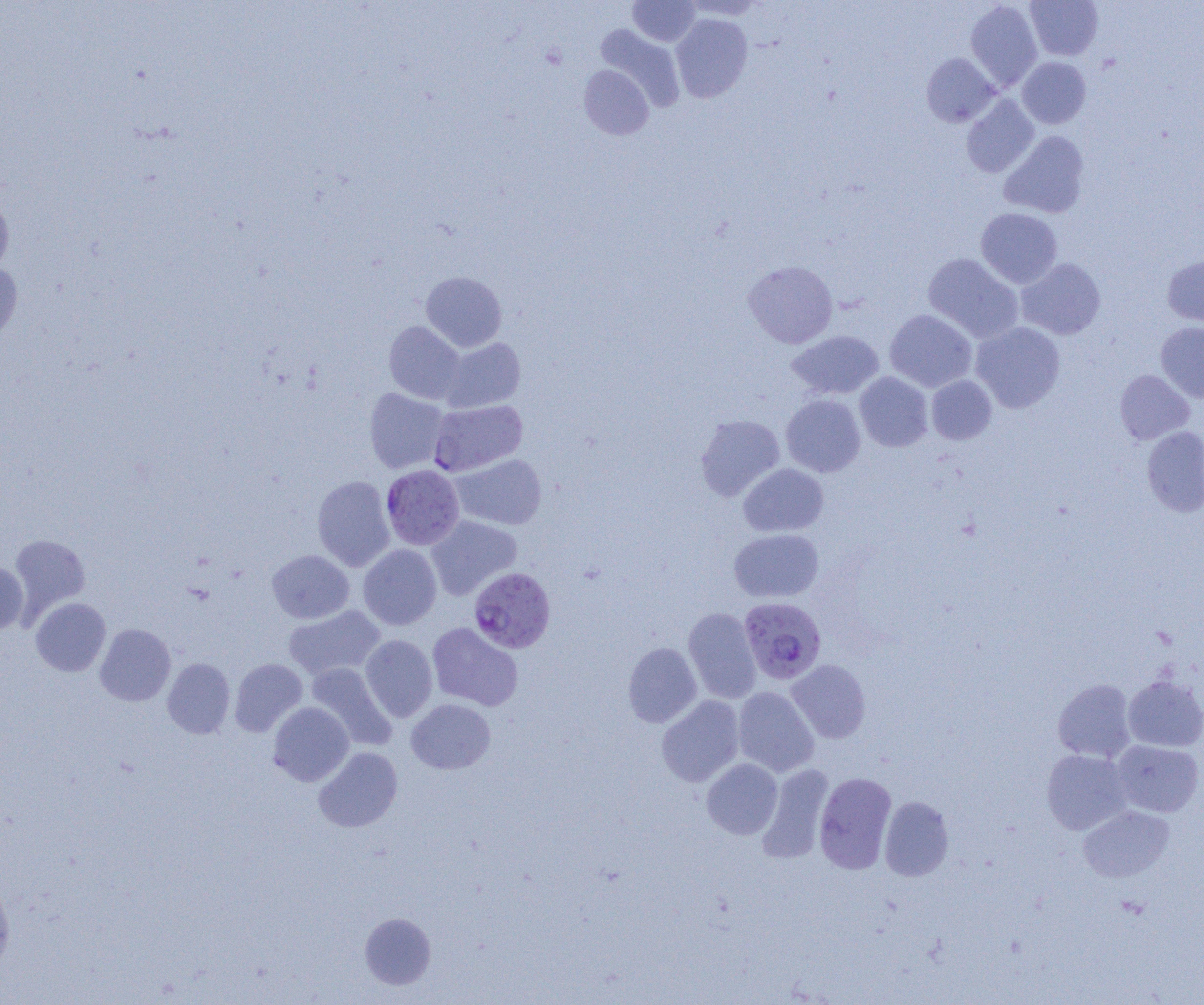

Summary:
  - Coordinate format: approximate bounding boxes as named x1/y1/x2/y2 corners in pixels
  - Uninfected red blood cell locations (subset): (x1=681, y1=0, x2=765, y2=20), (x1=1025, y1=0, x2=1103, y2=60), (x1=628, y1=1, x2=701, y2=46), (x1=965, y1=1, x2=1043, y2=91), (x1=671, y1=13, x2=753, y2=102), (x1=595, y1=24, x2=685, y2=112), (x1=922, y1=52, x2=999, y2=127), (x1=1017, y1=57, x2=1091, y2=128), (x1=579, y1=65, x2=654, y2=139), (x1=962, y1=95, x2=1039, y2=178), (x1=999, y1=131, x2=1090, y2=218), (x1=0, y1=193, x2=14, y2=280), (x1=976, y1=207, x2=1063, y2=288), (x1=923, y1=253, x2=1024, y2=343), (x1=1162, y1=254, x2=1204, y2=328), (x1=1016, y1=258, x2=1106, y2=340), (x1=743, y1=260, x2=838, y2=348), (x1=0, y1=262, x2=23, y2=355), (x1=421, y1=271, x2=507, y2=351), (x1=884, y1=309, x2=977, y2=391), (x1=384, y1=321, x2=465, y2=404), (x1=971, y1=321, x2=1065, y2=413), (x1=1155, y1=321, x2=1204, y2=403), (x1=786, y1=330, x2=884, y2=400), (x1=440, y1=338, x2=525, y2=412), (x1=1115, y1=369, x2=1194, y2=444), (x1=855, y1=372, x2=933, y2=451), (x1=926, y1=375, x2=997, y2=444), (x1=364, y1=388, x2=448, y2=473), (x1=781, y1=394, x2=865, y2=477), (x1=695, y1=414, x2=785, y2=501), (x1=1142, y1=425, x2=1204, y2=517), (x1=451, y1=454, x2=547, y2=530), (x1=738, y1=463, x2=828, y2=537), (x1=312, y1=475, x2=395, y2=571), (x1=426, y1=515, x2=522, y2=600), (x1=729, y1=529, x2=824, y2=603), (x1=9, y1=533, x2=90, y2=619), (x1=358, y1=544, x2=441, y2=630), (x1=267, y1=550, x2=354, y2=623), (x1=0, y1=561, x2=29, y2=633), (x1=30, y1=597, x2=111, y2=676), (x1=283, y1=605, x2=385, y2=680), (x1=683, y1=607, x2=762, y2=703), (x1=427, y1=622, x2=523, y2=711), (x1=95, y1=623, x2=175, y2=706), (x1=360, y1=635, x2=438, y2=721), (x1=623, y1=642, x2=702, y2=727), (x1=162, y1=658, x2=235, y2=738), (x1=230, y1=658, x2=307, y2=736), (x1=787, y1=660, x2=871, y2=743), (x1=306, y1=663, x2=396, y2=750), (x1=1124, y1=676, x2=1204, y2=751), (x1=1053, y1=678, x2=1136, y2=762), (x1=733, y1=686, x2=819, y2=776), (x1=657, y1=696, x2=744, y2=786), (x1=406, y1=698, x2=495, y2=774), (x1=268, y1=702, x2=354, y2=786), (x1=1112, y1=740, x2=1203, y2=817), (x1=314, y1=747, x2=403, y2=832), (x1=1041, y1=749, x2=1133, y2=835), (x1=702, y1=758, x2=782, y2=839), (x1=758, y1=764, x2=835, y2=863), (x1=814, y1=771, x2=897, y2=873), (x1=880, y1=796, x2=953, y2=881), (x1=1078, y1=805, x2=1174, y2=882), (x1=0, y1=875, x2=15, y2=976), (x1=360, y1=912, x2=436, y2=990)
  - Plasmodium falciparum-infected red blood cell locations (subset): (x1=381, y1=465, x2=464, y2=549), (x1=469, y1=567, x2=555, y2=653), (x1=739, y1=597, x2=826, y2=684)
  - Slide-level diagnosis: Plasmodium falciparum
  - Magnification: 1000x
  - Preparation: thin blood film
  - Field of view: one of a larger specimen
  - Modality: light microscopy
  - Image size: 1204×1005 pixels